Give the position of every Plasmodium parasite visible.
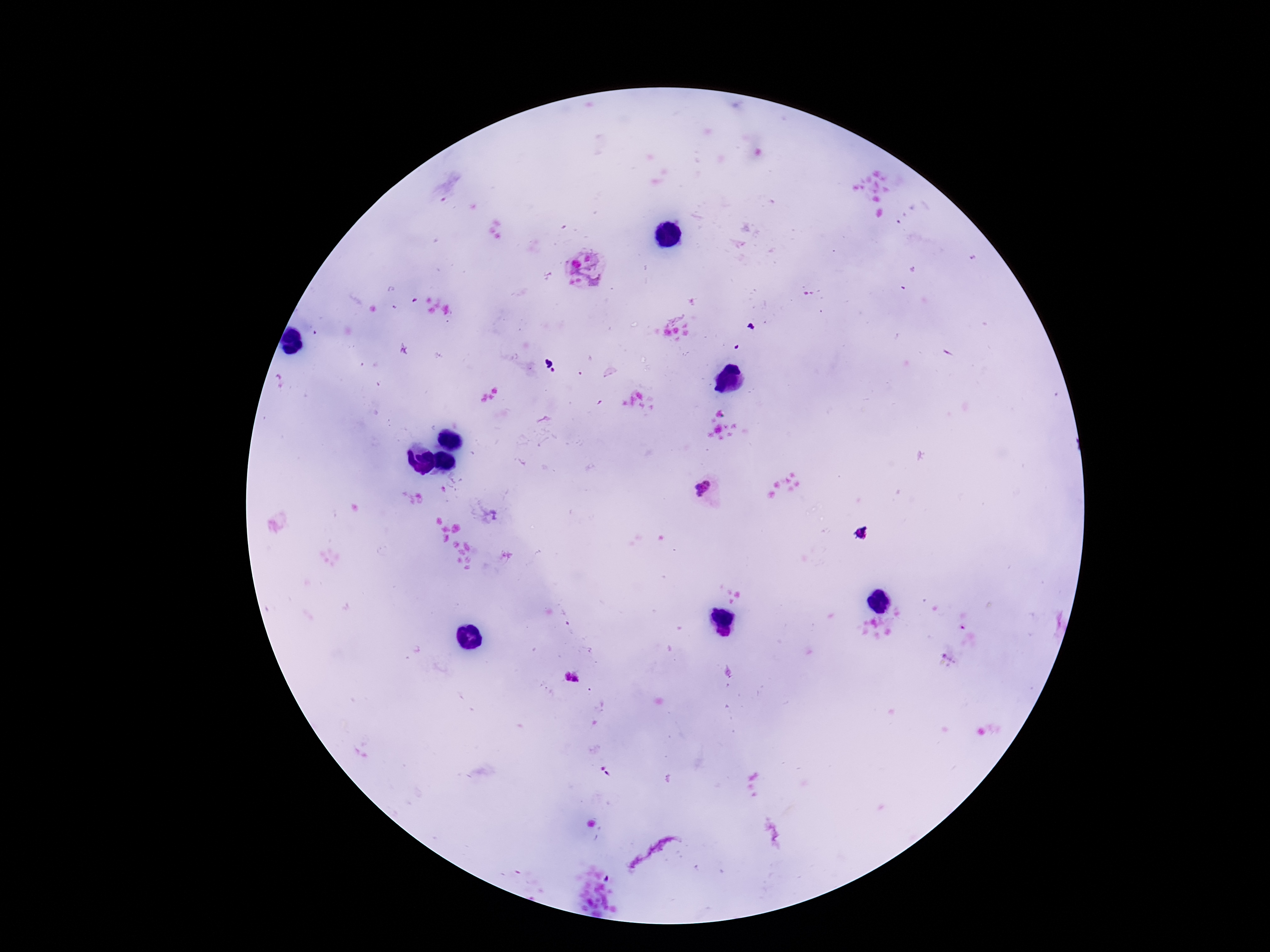
Approximate centers as [x, y] in pixels.
Plasmodium parasites: [586, 270], [707, 491], [605, 771].

preparation = thick blood film
capture = smartphone camera through the microscope eyepiece
field of view = one from this slide
magnification = 100x
stain = Giemsa
patient malaria status = infected
image size = 1270×952 pixels